Point out each leukocyte.
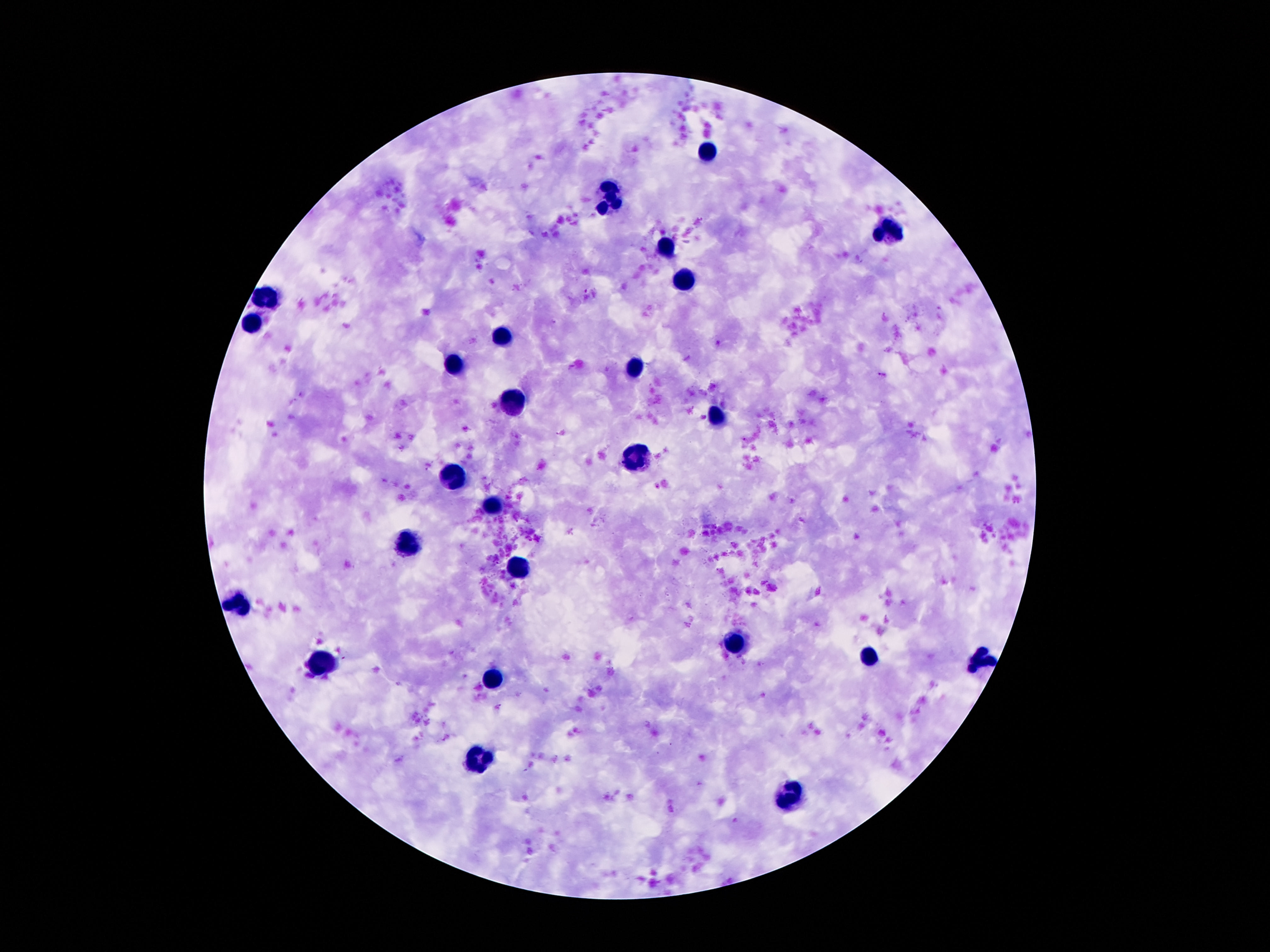

Approximate centers as [x, y] in pixels.
Leukocytes: [711, 150], [610, 197], [890, 230], [666, 248], [684, 280], [270, 297], [255, 325], [503, 334], [461, 364], [632, 364], [513, 403], [720, 413], [638, 456], [453, 476], [494, 504], [412, 544], [517, 566], [240, 606], [737, 641], [869, 660], [983, 661], [319, 664], [494, 679], [477, 763], [789, 795].

patient malaria status = negative
magnification = 100x
image size = 1270×952 pixels
capture = smartphone camera through the microscope eyepiece
field of view = single
preparation = thick peripheral-blood smear
stain = Giemsa